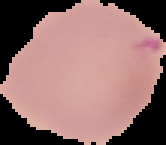
Summary:
  - Image size: 166×145 pixels
  - Preparation: thin blood smear
  - Result: no malaria parasites seen
  - Image type: segmented cell region with the area outside set to black